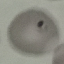

Summary:
  - Malaria status: uninfected
  - Image type: automatically extracted cell patch, resized to 64 × 64 pixels
  - Preparation: thin blood smear
  - Stain: Giemsa
  - Capture: smartphone through the microscope eyepiece